Assess this cell for malaria.
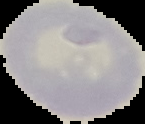
Uninfected.

From a thin blood smear. Segmented cell region on a black background. Image is 145×124 pixels.